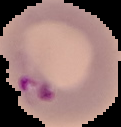

From a thin blood film. Result: Plasmodium parasites detected. Image is 121×127 pixels. Cell region segmented out of the field of view; the surrounding area is masked to black.